Comment on the morphology of the red blood cells.
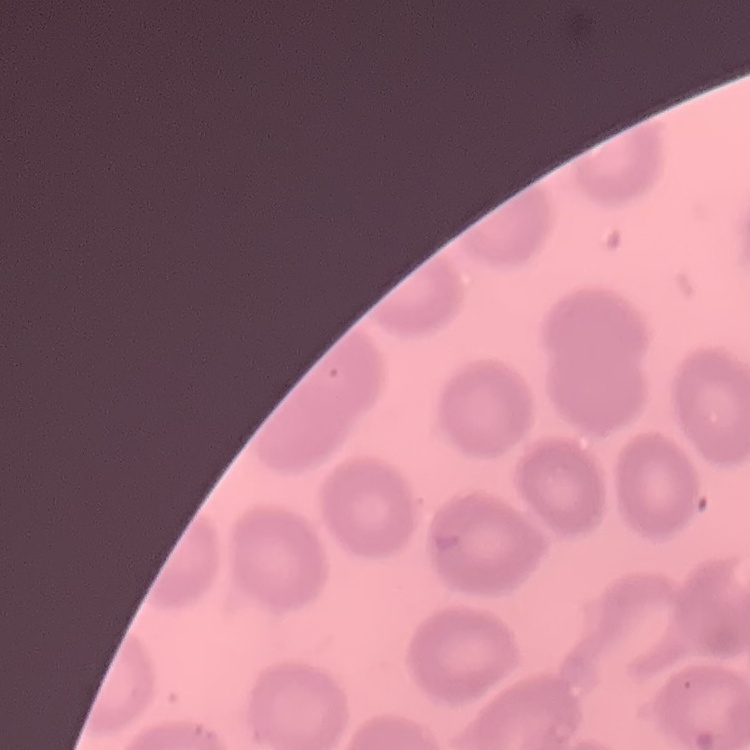
They show no rouleaux formation.

preparation: thin blood smear
image_type: one tile cut from a larger photomicrograph
stain: Field's or Giemsa